Locate and identify every blood parasite.
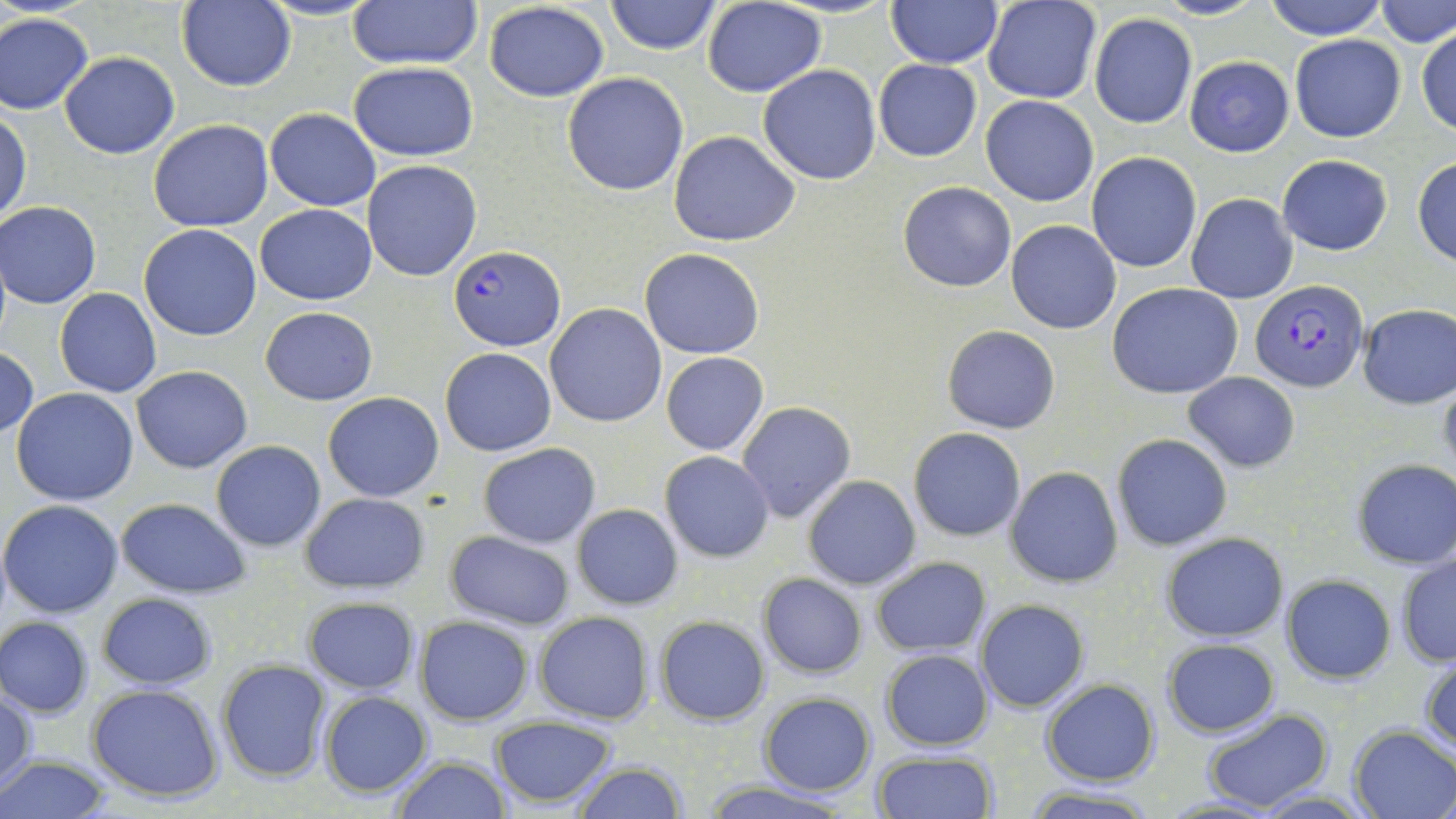

Approximate bounding boxes as (x1,y1)-(x2,y2) corner pairs in pixels.
Plasmodium falciparum-infected red blood cells: (448,245)-(564,351), (1248,278)-(1368,391).
No Plasmodium ovale, Plasmodium malariae, Plasmodium vivax, Babesia divergens, or Trypanosoma brucei observed.

{
  "slide_level_diagnosis": "Plasmodium falciparum",
  "stain": "May-Grünwald-Giemsa",
  "modality": "light microscopy",
  "preparation": "thin blood smear",
  "uninfected_red_blood_cell_locations": "approximate bounding boxes as (x1,y1)-(x2,y2) corner pairs in pixels: (347,0)-(482,70), (604,0)-(722,55), (1150,0)-(1265,21), (1262,0)-(1389,40), (1377,0)-(1456,48), (175,1)-(296,91), (702,1)-(826,97), (885,1)-(1002,68), (484,2)-(611,102), (982,2)-(1102,105), (0,12)-(94,114), (1088,13)-(1198,128), (1416,26)-(1456,135), (1290,34)-(1406,142), (59,52)-(180,158), (1185,55)-(1294,156), (873,59)-(981,161), (349,62)-(478,162), (757,64)-(883,185), (562,73)-(688,195), (980,95)-(1098,207), (264,108)-(381,211), (1,110)-(30,224), (148,120)-(274,233), (669,131)-(801,245), (1086,151)-(1202,273), (1277,155)-(1393,255), (1412,156)-(1456,267), (362,161)-(484,282), (898,181)-(1015,291), (1187,193)-(1297,303), (1,201)-(102,309), (256,203)-(377,306), (1006,221)-(1122,334), (139,223)-(262,342), (640,248)-(765,360), (1107,283)-(1245,399), (55,288)-(161,396), (545,303)-(667,427), (1358,303)-(1456,409), (261,307)-(377,405), (942,325)-(1062,434), (0,347)-(38,439), (440,347)-(555,456), (660,352)-(769,455), (131,365)-(253,473), (1183,371)-(1300,472), (1438,374)-(1456,483), (11,388)-(139,504), (323,391)-(444,501), (736,401)-(856,522), (908,427)-(1026,541), (1111,433)-(1233,552), (209,440)-(326,552), (477,442)-(601,547), (660,451)-(775,562), (1350,459)-(1456,568), (1005,465)-(1124,588), (802,474)-(920,590), (300,492)-(430,594), (116,498)-(252,598), (1,499)-(123,618), (571,503)-(683,609), (446,531)-(576,631), (1160,533)-(1288,641), (1396,553)-(1455,667), (871,556)-(991,657), (758,573)-(867,678), (1282,574)-(1396,683), (96,594)-(217,688), (302,596)-(420,695), (974,600)-(1089,713), (533,610)-(654,724), (654,615)-(770,724), (416,616)-(533,725), (1,617)-(92,718), (1162,639)-(1280,738), (880,648)-(993,750), (1420,653)-(1456,755), (216,659)-(332,783), (1040,681)-(1161,784), (87,683)-(226,802), (1,687)-(35,794), (319,690)-(432,798), (759,693)-(877,795), (1200,708)-(1334,812), (487,716)-(620,808), (1349,725)-(1456,818), (871,748)-(997,819), (390,754)-(511,819), (0,755)-(112,819), (569,761)-(690,818), (696,781)-(861,818), (1018,786)-(1165,818), (1252,789)-(1372,818)",
  "field_of_view": "single",
  "image_size": "1456×819 pixels",
  "magnification": "1000x"
}